Comment on the morphology of the red blood cells.
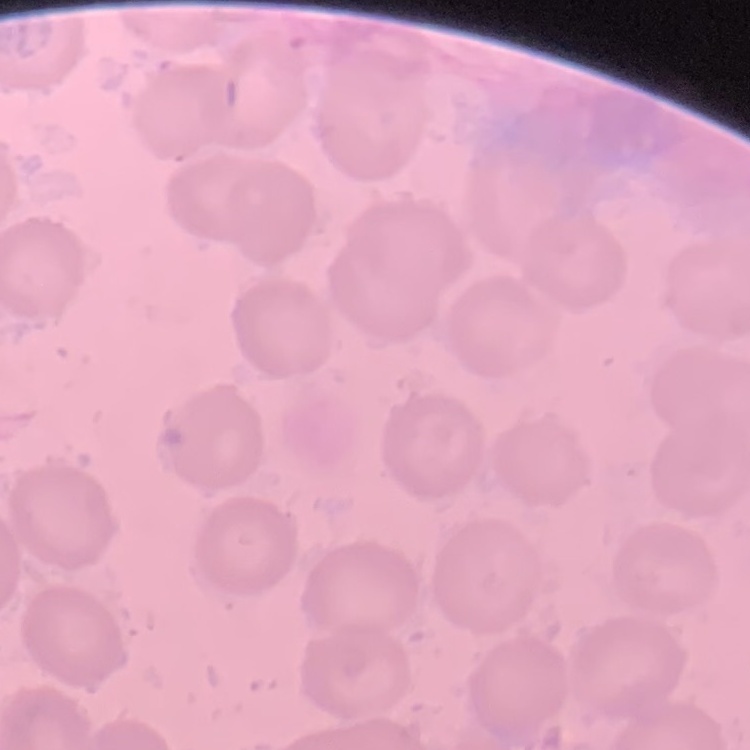

They show no rouleaux formation.

Summary:
  - Stain: Field's or Giemsa
  - Image type: square crop of a larger photomicrograph
  - Preparation: thin blood smear